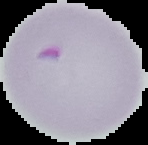

preparation = thin blood film
malaria status = parasitized
image type = segmented cell region with the area outside set to black
image size = 148×145 pixels